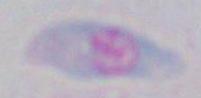

Summary:
  - Magnification: 1000x
  - Modality: micrograph
  - Identification: Toxoplasma gondii